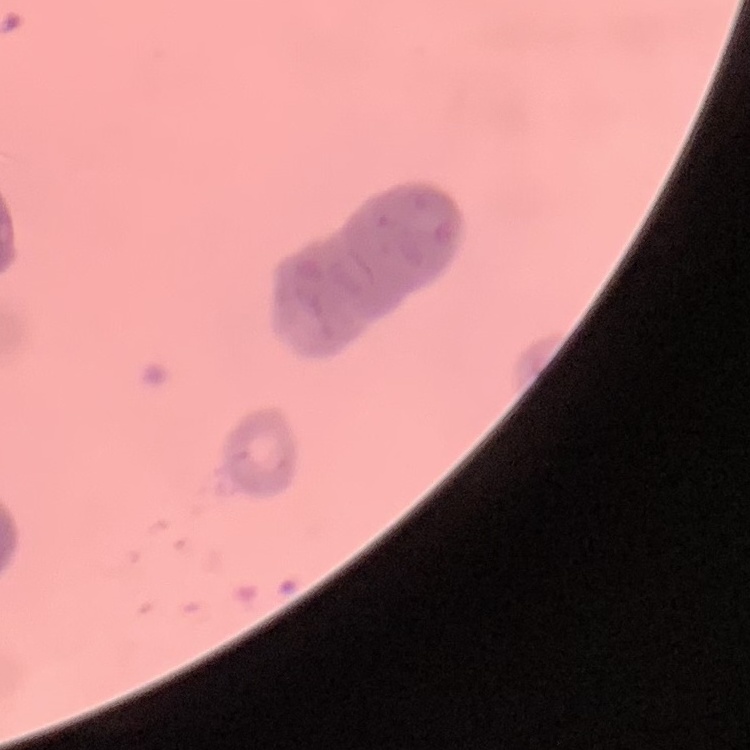

The erythrocytes show rouleaux formation. One tile cut from a larger photomicrograph. Stained with either Field's or Giemsa. Thin blood film.